Assess this cell for malaria.
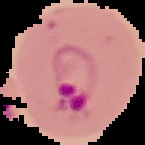

It is parasitized.

{
  "preparation": "thin blood film",
  "image_size": "145×145 pixels",
  "image_type": "cell region segmented out of the field of view; surrounding area masked to black"
}